Assess this cell for malaria.
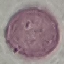

It is uninfected.

Acquired by smartphone through the microscope eyepiece. Thin smear of blood. Giemsa stain. Cell patch, automatically extracted from a larger field of view and resized to 64 × 64 pixels.